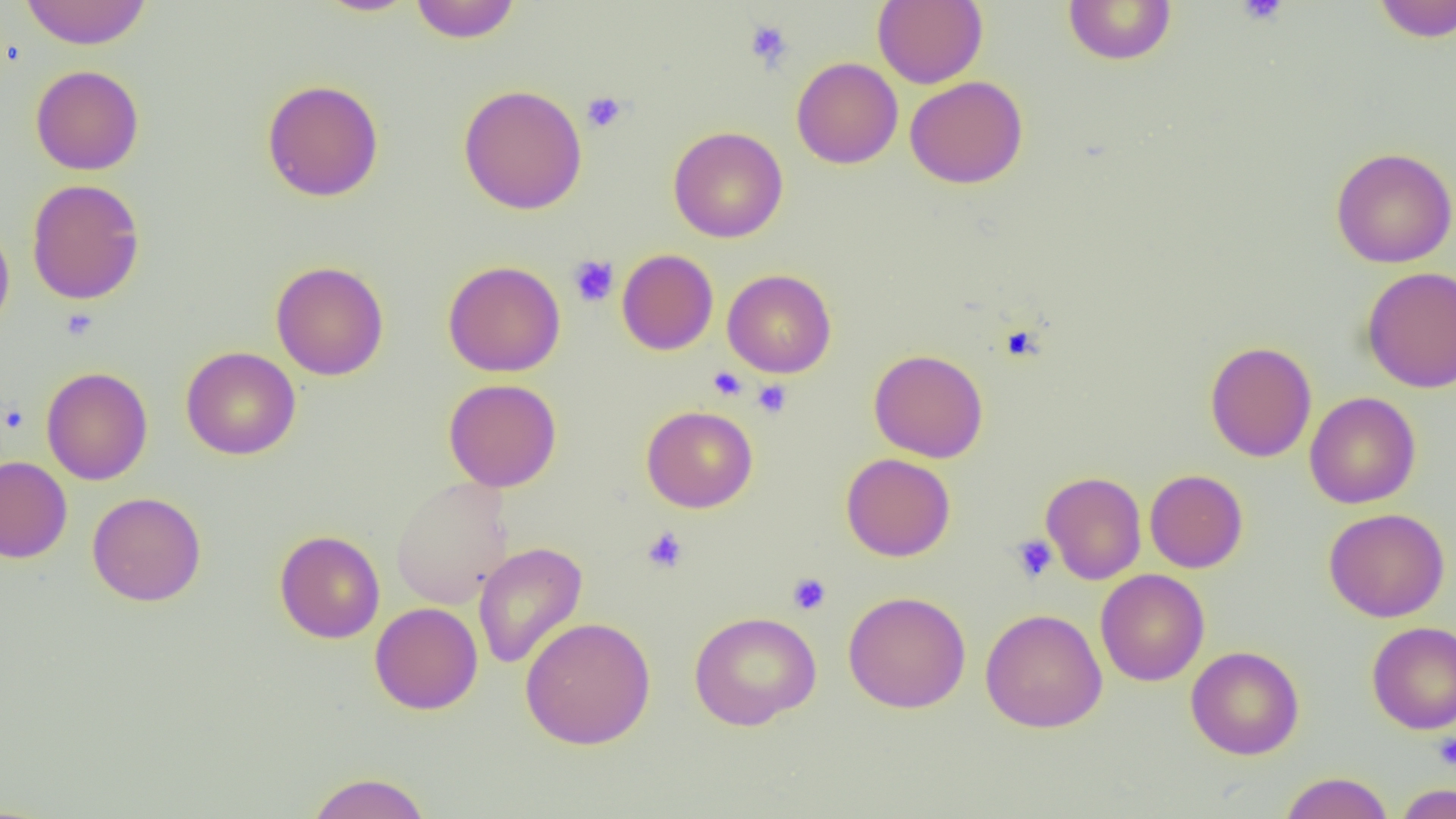

Summary:
  - Coordinate format: approximate bounding boxes as (x1,y1)-(x2,y2) corner pairs in pixels
  - Platelet locations: (1236,0)-(1289,25), (744,20)-(793,70), (581,91)-(627,133), (568,255)-(619,307), (708,367)-(747,401), (751,379)-(792,418), (2,405)-(28,433), (641,526)-(689,574), (1010,534)-(1058,583), (787,573)-(831,615), (1433,732)-(1456,771)
  - Uninfected red blood cell locations: (19,0)-(153,49), (314,0)-(421,17), (409,0)-(521,43), (872,0)-(987,88), (1063,0)-(1177,65), (1371,0)-(1456,42), (791,57)-(903,170), (30,65)-(144,175), (905,76)-(1028,189), (261,79)-(384,202), (458,84)-(587,215), (668,125)-(788,243), (1330,146)-(1455,268), (27,179)-(145,305), (0,219)-(15,337), (617,249)-(718,355), (443,260)-(566,377), (270,261)-(389,380), (1362,266)-(1456,393), (722,269)-(836,377), (1205,341)-(1317,462), (181,346)-(301,460), (868,349)-(989,463), (41,367)-(153,485), (443,378)-(562,492), (1304,392)-(1421,509), (642,405)-(758,512), (841,453)-(956,561), (0,456)-(72,563), (1144,469)-(1248,573), (1041,471)-(1147,584), (391,476)-(513,608), (87,491)-(206,606), (1323,507)-(1450,623), (275,530)-(385,643), (473,541)-(588,670), (1095,569)-(1210,686), (843,590)-(971,713), (370,602)-(483,715), (981,608)-(1108,733), (689,610)-(821,730), (520,616)-(656,750), (1366,621)-(1456,734), (1186,646)-(1304,759), (306,771)-(432,818), (1279,771)-(1394,819), (1394,782)-(1455,819)
  - Slide-level diagnosis: no evidence of blood parasites
  - Image size: 1456×819 pixels
  - Modality: optical microscopy
  - Preparation: thin blood film
  - Magnification: 1000x
  - Field of view: one of a larger specimen